Classify this cell by malaria status.
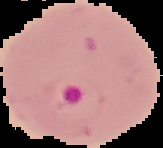

Parasitized.

Image is 163×148 pixels. From a thin blood film. The area outside the segmented cell region is set to black.